Name the blood parasite species.
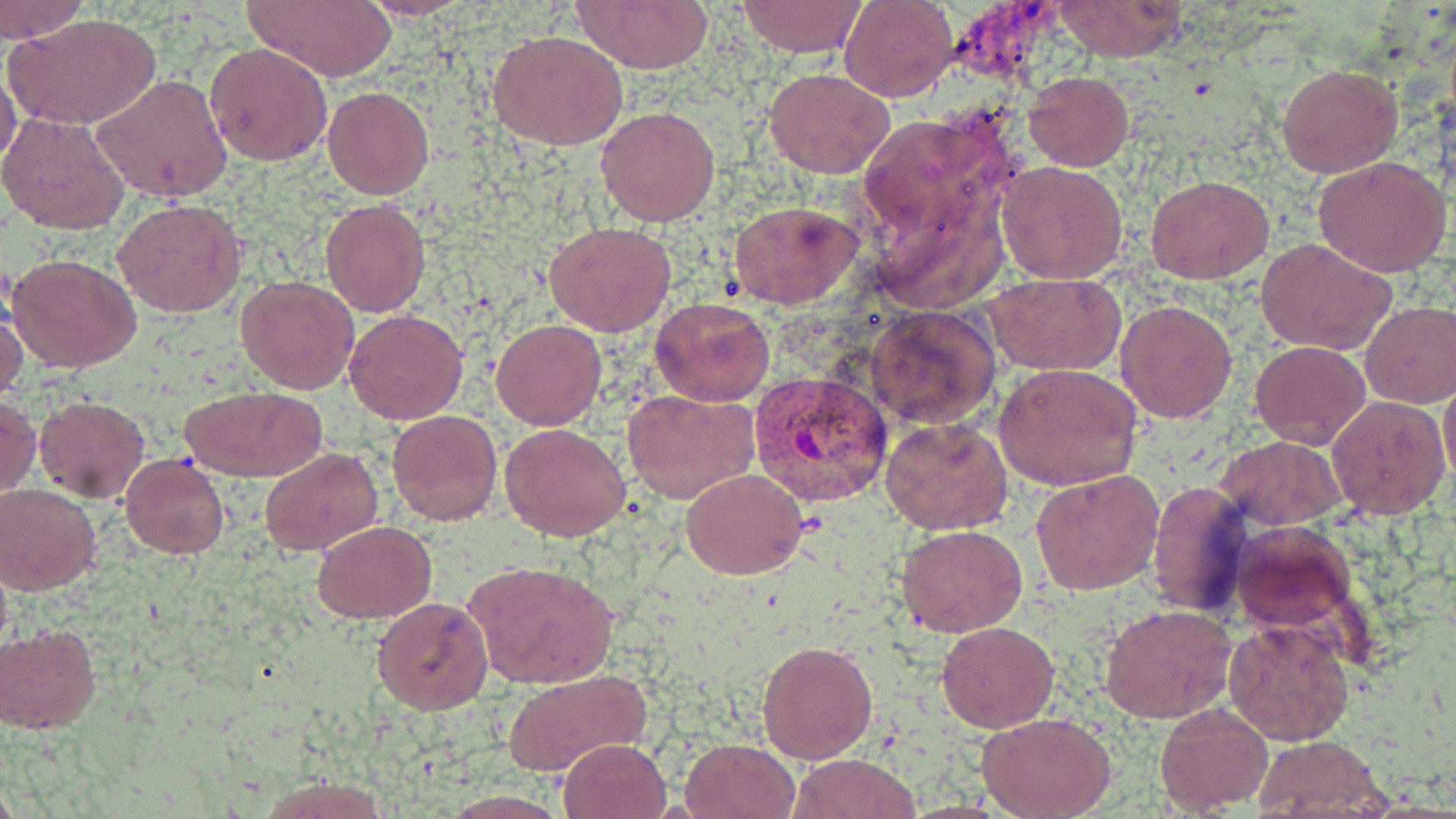
Plasmodium vivax.

Approximate bounding boxes as named x1/y1/x2/y2 corners in pixels. Uninfected red blood cell locations: (x1=241, y1=0, x2=395, y2=84), (x1=361, y1=0, x2=473, y2=20), (x1=572, y1=0, x2=713, y2=73), (x1=0, y1=1, x2=89, y2=42), (x1=736, y1=1, x2=868, y2=56), (x1=839, y1=1, x2=958, y2=101), (x1=1050, y1=1, x2=1191, y2=63), (x1=10, y1=15, x2=159, y2=131), (x1=489, y1=29, x2=628, y2=150), (x1=205, y1=42, x2=333, y2=167), (x1=1, y1=61, x2=22, y2=178), (x1=1277, y1=63, x2=1402, y2=178), (x1=764, y1=68, x2=894, y2=179), (x1=1025, y1=71, x2=1133, y2=171), (x1=92, y1=73, x2=234, y2=203), (x1=323, y1=86, x2=433, y2=199), (x1=595, y1=105, x2=721, y2=226), (x1=856, y1=106, x2=1024, y2=268), (x1=0, y1=110, x2=131, y2=233), (x1=1314, y1=156, x2=1455, y2=277), (x1=997, y1=160, x2=1128, y2=283), (x1=1147, y1=176, x2=1274, y2=284), (x1=323, y1=199, x2=429, y2=316), (x1=112, y1=200, x2=246, y2=319), (x1=729, y1=200, x2=861, y2=310), (x1=544, y1=221, x2=676, y2=336), (x1=1256, y1=238, x2=1395, y2=355), (x1=8, y1=253, x2=143, y2=372), (x1=983, y1=273, x2=1125, y2=376), (x1=237, y1=276, x2=360, y2=393), (x1=649, y1=296, x2=775, y2=405), (x1=1115, y1=299, x2=1237, y2=422), (x1=1360, y1=301, x2=1456, y2=408), (x1=864, y1=302, x2=1002, y2=431), (x1=0, y1=303, x2=29, y2=405), (x1=345, y1=310, x2=468, y2=426), (x1=492, y1=319, x2=605, y2=431), (x1=1250, y1=340, x2=1370, y2=449), (x1=995, y1=363, x2=1143, y2=489), (x1=1439, y1=374, x2=1456, y2=485), (x1=177, y1=384, x2=326, y2=483), (x1=622, y1=390, x2=758, y2=504), (x1=0, y1=393, x2=41, y2=496), (x1=1327, y1=394, x2=1451, y2=520), (x1=34, y1=396, x2=151, y2=501), (x1=387, y1=411, x2=501, y2=526), (x1=881, y1=418, x2=1012, y2=536), (x1=500, y1=423, x2=631, y2=540), (x1=1217, y1=435, x2=1348, y2=529), (x1=260, y1=448, x2=383, y2=556), (x1=120, y1=454, x2=229, y2=559), (x1=1031, y1=467, x2=1166, y2=595), (x1=681, y1=468, x2=807, y2=579), (x1=1148, y1=479, x2=1253, y2=617), (x1=0, y1=484, x2=101, y2=592), (x1=311, y1=520, x2=437, y2=620), (x1=1232, y1=520, x2=1358, y2=633), (x1=897, y1=526, x2=1026, y2=638), (x1=463, y1=559, x2=619, y2=689), (x1=372, y1=596, x2=493, y2=715), (x1=1099, y1=603, x2=1236, y2=725), (x1=1224, y1=618, x2=1354, y2=745), (x1=937, y1=622, x2=1058, y2=733), (x1=0, y1=623, x2=102, y2=733), (x1=758, y1=639, x2=878, y2=763), (x1=502, y1=667, x2=650, y2=778), (x1=1154, y1=703, x2=1274, y2=814), (x1=978, y1=713, x2=1117, y2=819), (x1=1249, y1=733, x2=1388, y2=817), (x1=558, y1=737, x2=672, y2=819), (x1=681, y1=737, x2=800, y2=819), (x1=792, y1=753, x2=922, y2=818). Plasmodium vivax-infected red blood cell locations: (x1=750, y1=371, x2=894, y2=508). Optical microscopy. 1000x magnification. Thin blood smear. May-Grünwald-Giemsa-stained preparation. Image is 1456×819 pixels. Single field of view.